Classify this cell by malaria status.
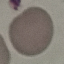
It is uninfected.

preparation = thin smear
image type = automatically extracted cell patch, resized to 64 × 64 pixels
capture = smartphone camera at the microscope eyepiece
stain = Giemsa